Report the malaria status of this cell.
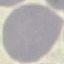

It is uninfected.

Summary:
  - Image type: automatically extracted cell patch, resized to 64 × 64 pixels
  - Stain: Giemsa
  - Preparation: thin smear
  - Capture: smartphone camera at the microscope eyepiece